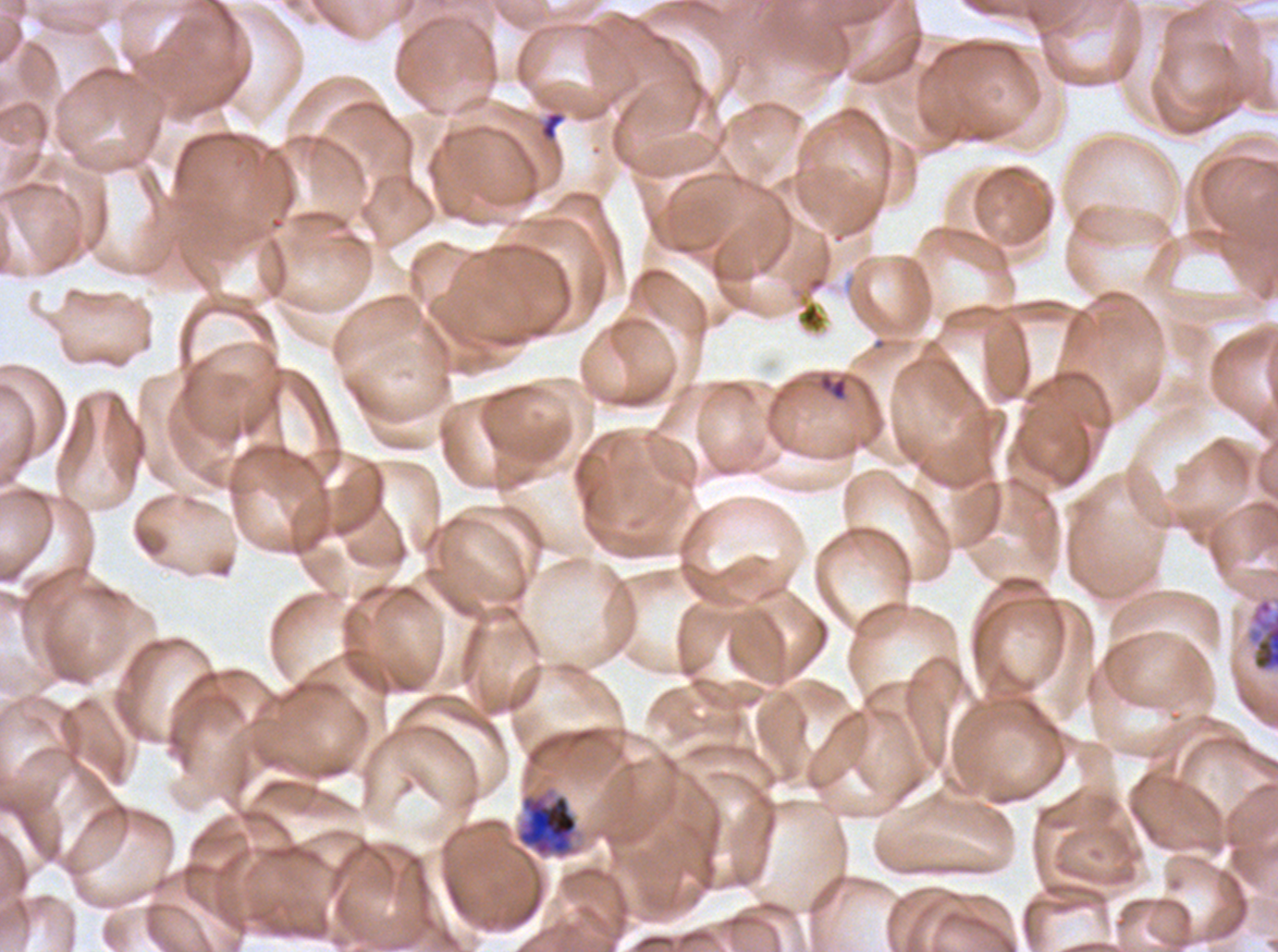
Approximate bounding boxes as [x1, y1, x2, y2] in pixels. Debris locations: [538, 110, 567, 142]. Ring locations: [818, 374, 848, 401]. Early schizont locations: [1247, 597, 1277, 673], [515, 787, 579, 860]. One sub-image of a larger composite. Thin blood smear. Image is 1278×952 pixels. Life-cycle stages observed: ring, early schizont. Ex-vivo P. falciparum culture from a patient in The Gambia, grown for 24 to 48 hours. Giemsa stain.